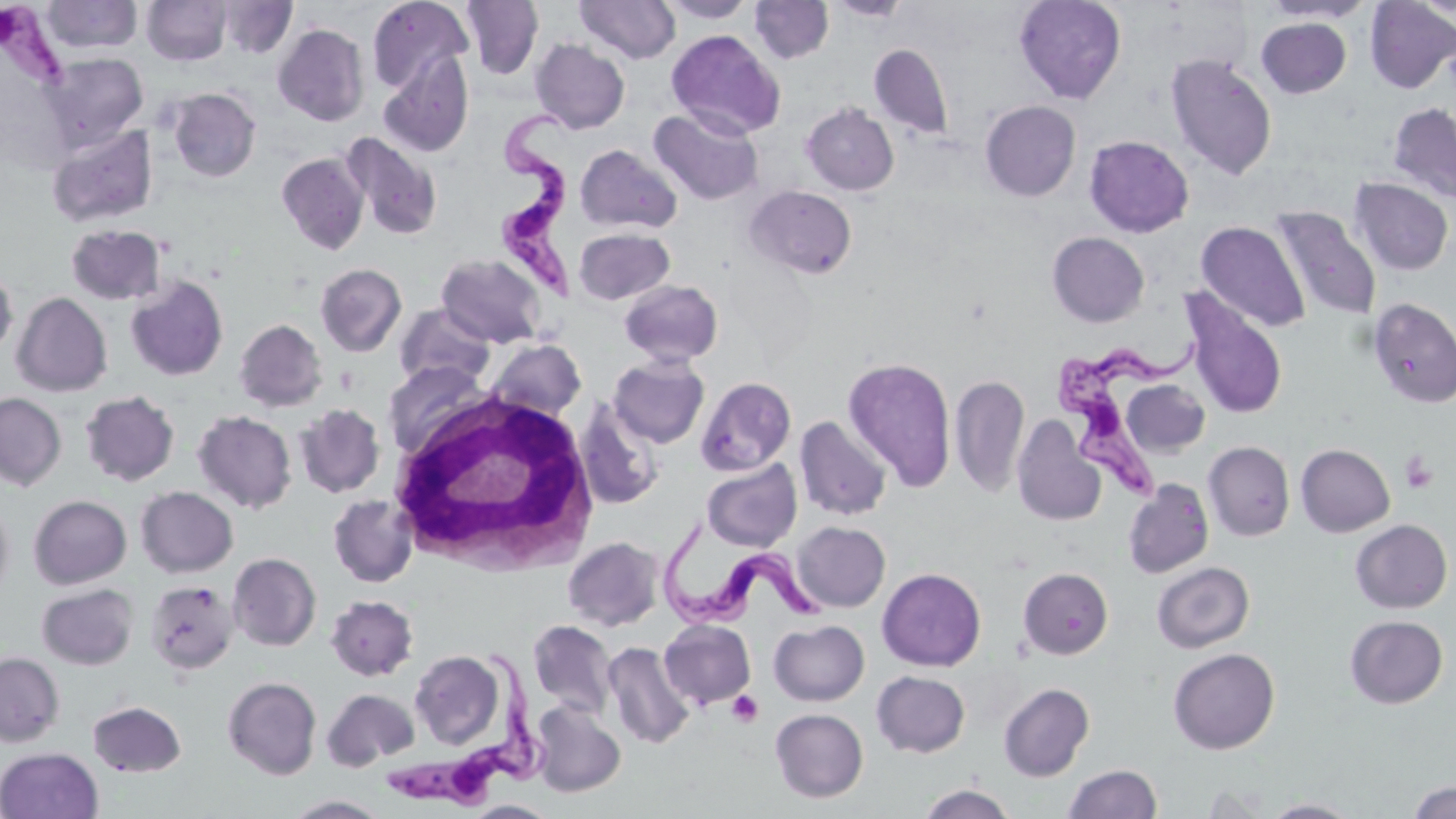
Summary:
  - Coordinate format: approximate bounding boxes as named x1/y1/x2/y2 corners in pixels
  - Uninfected red blood cell locations: (x1=41, y1=0, x2=143, y2=54), (x1=367, y1=0, x2=474, y2=94), (x1=575, y1=0, x2=681, y2=64), (x1=656, y1=0, x2=759, y2=22), (x1=827, y1=0, x2=913, y2=21), (x1=1014, y1=0, x2=1127, y2=104), (x1=1261, y1=0, x2=1376, y2=23), (x1=142, y1=1, x2=231, y2=66), (x1=219, y1=1, x2=297, y2=58), (x1=461, y1=1, x2=544, y2=80), (x1=750, y1=1, x2=834, y2=64), (x1=1365, y1=1, x2=1456, y2=93), (x1=1256, y1=18, x2=1351, y2=98), (x1=273, y1=25, x2=370, y2=125), (x1=666, y1=29, x2=785, y2=139), (x1=531, y1=39, x2=630, y2=133), (x1=869, y1=43, x2=954, y2=139), (x1=378, y1=52, x2=474, y2=158), (x1=42, y1=53, x2=148, y2=151), (x1=1166, y1=54, x2=1278, y2=180), (x1=168, y1=88, x2=261, y2=182), (x1=980, y1=100, x2=1080, y2=201), (x1=802, y1=102, x2=899, y2=195), (x1=1388, y1=102, x2=1456, y2=203), (x1=649, y1=107, x2=763, y2=206), (x1=47, y1=124, x2=158, y2=228), (x1=341, y1=133, x2=441, y2=240), (x1=1084, y1=135, x2=1194, y2=237), (x1=575, y1=144, x2=682, y2=234), (x1=276, y1=152, x2=371, y2=254), (x1=1350, y1=177, x2=1454, y2=275), (x1=745, y1=185, x2=857, y2=280), (x1=1270, y1=206, x2=1381, y2=322), (x1=1196, y1=221, x2=1311, y2=332), (x1=66, y1=224, x2=167, y2=305), (x1=574, y1=228, x2=675, y2=305), (x1=1047, y1=232, x2=1149, y2=327), (x1=435, y1=253, x2=549, y2=348), (x1=315, y1=263, x2=407, y2=357), (x1=0, y1=266, x2=17, y2=359), (x1=125, y1=275, x2=228, y2=381), (x1=619, y1=279, x2=724, y2=366), (x1=12, y1=292, x2=112, y2=397), (x1=1182, y1=292, x2=1287, y2=420), (x1=1368, y1=298, x2=1456, y2=408), (x1=394, y1=303, x2=496, y2=389), (x1=235, y1=319, x2=328, y2=411), (x1=487, y1=339, x2=586, y2=421), (x1=608, y1=355, x2=709, y2=448), (x1=842, y1=356, x2=957, y2=492), (x1=384, y1=360, x2=491, y2=458), (x1=950, y1=374, x2=1029, y2=497), (x1=695, y1=376, x2=796, y2=476), (x1=1121, y1=380, x2=1210, y2=458), (x1=80, y1=390, x2=180, y2=486), (x1=0, y1=392, x2=66, y2=491), (x1=574, y1=401, x2=664, y2=510), (x1=294, y1=404, x2=385, y2=497), (x1=193, y1=410, x2=297, y2=513), (x1=794, y1=415, x2=891, y2=521), (x1=1011, y1=415, x2=1106, y2=527), (x1=1203, y1=441, x2=1295, y2=541), (x1=1295, y1=443, x2=1395, y2=537), (x1=701, y1=459, x2=802, y2=551), (x1=1122, y1=478, x2=1214, y2=579), (x1=135, y1=486, x2=238, y2=577), (x1=328, y1=493, x2=418, y2=588), (x1=29, y1=494, x2=131, y2=589), (x1=0, y1=498, x2=14, y2=602), (x1=1350, y1=519, x2=1452, y2=613), (x1=793, y1=521, x2=890, y2=611), (x1=563, y1=536, x2=663, y2=631), (x1=228, y1=552, x2=321, y2=651), (x1=1151, y1=561, x2=1255, y2=653), (x1=877, y1=567, x2=986, y2=671), (x1=1019, y1=567, x2=1113, y2=659), (x1=145, y1=579, x2=239, y2=675), (x1=37, y1=583, x2=138, y2=670), (x1=325, y1=595, x2=418, y2=681), (x1=1345, y1=615, x2=1448, y2=708), (x1=660, y1=619, x2=756, y2=709), (x1=769, y1=619, x2=869, y2=706), (x1=528, y1=620, x2=617, y2=718), (x1=603, y1=641, x2=695, y2=749), (x1=1168, y1=647, x2=1280, y2=754), (x1=410, y1=650, x2=506, y2=749), (x1=0, y1=652, x2=64, y2=746), (x1=871, y1=670, x2=970, y2=757), (x1=223, y1=676, x2=321, y2=779), (x1=998, y1=682, x2=1094, y2=781), (x1=322, y1=688, x2=419, y2=771), (x1=529, y1=700, x2=626, y2=797), (x1=87, y1=701, x2=186, y2=777), (x1=770, y1=708, x2=868, y2=803), (x1=0, y1=747, x2=103, y2=819), (x1=1063, y1=764, x2=1162, y2=819), (x1=1407, y1=780, x2=1456, y2=819), (x1=916, y1=784, x2=1018, y2=819), (x1=283, y1=794, x2=391, y2=818), (x1=1262, y1=798, x2=1362, y2=818), (x1=463, y1=800, x2=559, y2=819)
  - Trypanosoma brucei locations: (x1=0, y1=3, x2=74, y2=94), (x1=499, y1=104, x2=587, y2=309), (x1=1055, y1=326, x2=1211, y2=509), (x1=658, y1=511, x2=838, y2=636), (x1=383, y1=644, x2=562, y2=813)
  - Platelet locations: (x1=1400, y1=451, x2=1438, y2=495), (x1=727, y1=690, x2=764, y2=727)
  - White blood cell locations: (x1=387, y1=389, x2=601, y2=576)
  - Slide-level diagnosis: Trypanosoma brucei
  - Modality: optical microscopy
  - Field of view: single
  - Preparation: thin blood film
  - Magnification: 1000x
  - Stain: May-Grünwald-Giemsa
  - Image size: 1456×819 pixels